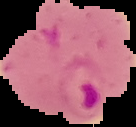
Summary:
  - Image size: 136×127 pixels
  - Image type: segmented cell region with the area outside set to black
  - Preparation: thin blood film
  - Malaria status: parasitized